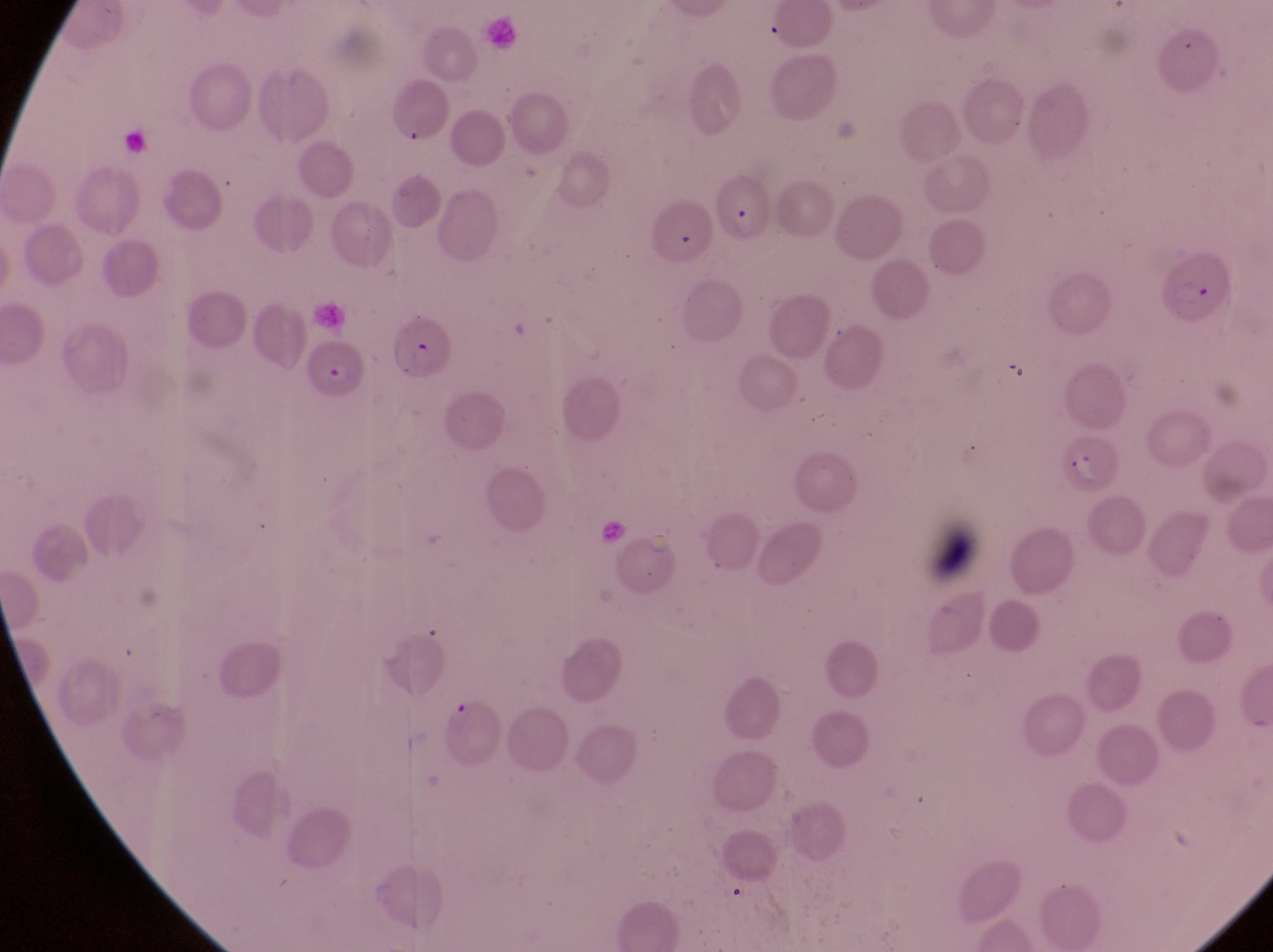

field of view = single
preparation = thin blood film
magnification = 1000x
parasitised red blood cell locations = approximate bounding boxes as (left, top, right, bottom) in pixels: (719, 175, 774, 245), (1155, 248, 1237, 330), (305, 340, 368, 405), (1055, 432, 1127, 502)
image size = 1273×952 pixels
capture = smartphone photograph through the eyepiece of an Olympus CX-23 microscope
country = Uganda